Assess this cell for malaria.
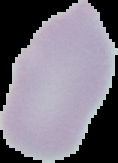
Uninfected.

{
  "image_type": "segmented cell region on a black background",
  "preparation": "thin blood film",
  "image_size": "118×163 pixels"
}